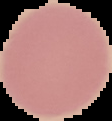 Malaria status: uninfected. Image is 112×121 pixels. Cell region segmented out of the field of view; the surrounding area is masked to black. From a thin blood smear.